Point out each leukocyte.
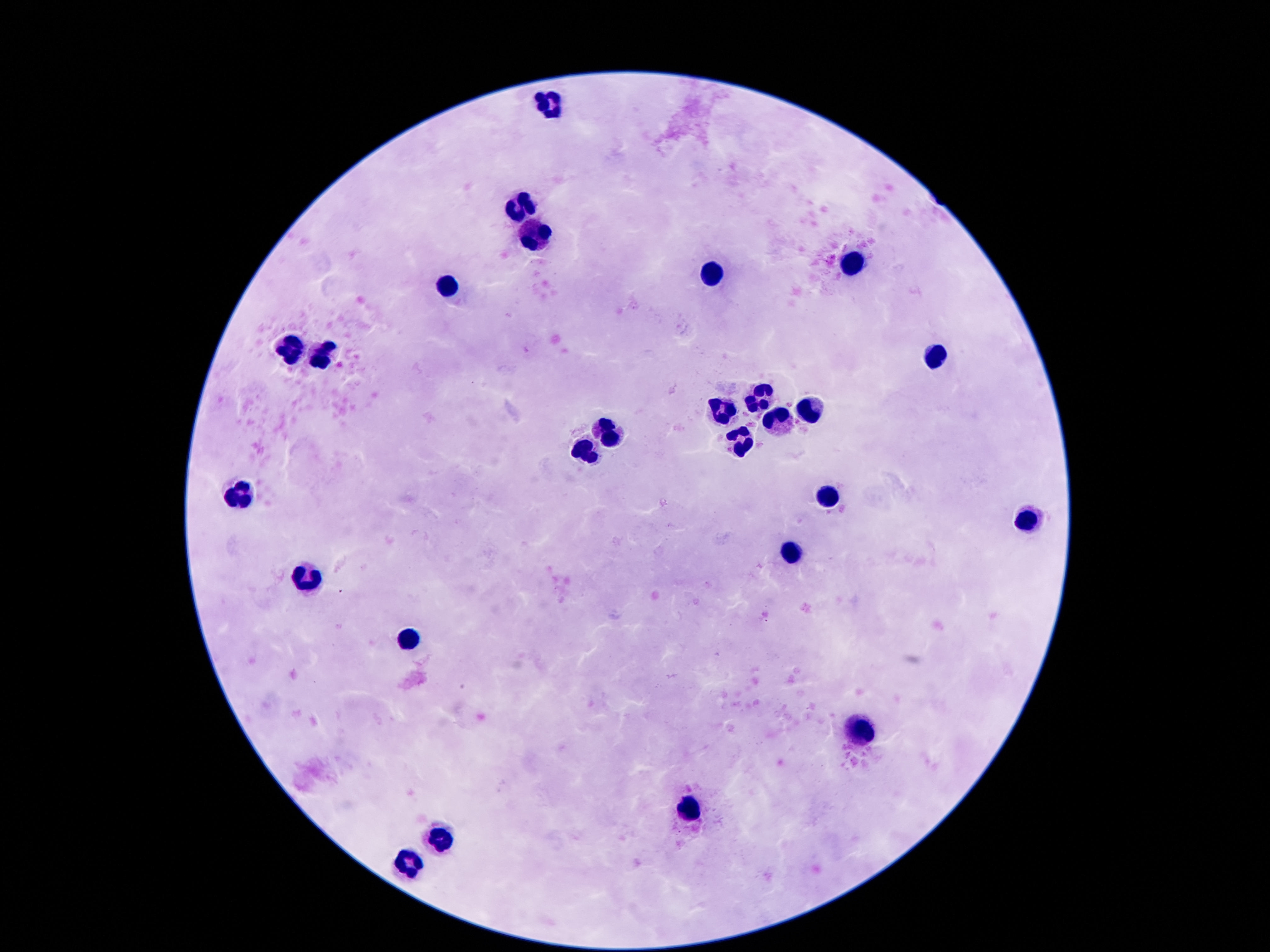
Approximate object centers, in pixels from the top-left corner.
Leukocytes: (x=550, y=103), (x=522, y=204), (x=536, y=230), (x=852, y=265), (x=718, y=272), (x=449, y=285), (x=289, y=349), (x=326, y=355), (x=942, y=355), (x=754, y=397), (x=723, y=406), (x=810, y=411), (x=774, y=416), (x=606, y=431), (x=740, y=437), (x=586, y=450), (x=242, y=493), (x=821, y=495), (x=1026, y=512), (x=793, y=551), (x=306, y=577), (x=407, y=641), (x=864, y=731), (x=690, y=809), (x=438, y=839), (x=413, y=859).

Image is 1270×952 pixels. Smartphone photograph taken through the microscope eyepiece. Patient malaria status: uninfected. Giemsa stain. Single field of view. 100x magnification. Thick blood smear.